Name the parasite shown.
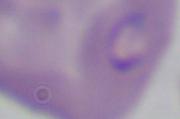
Babesia.

Micrograph. 1000x magnification.